Name the parasite shown.
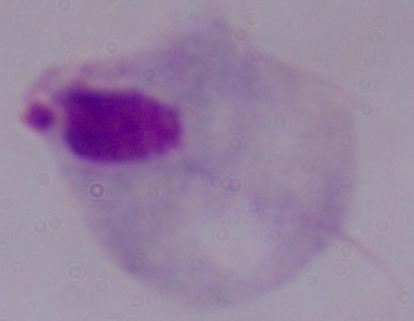

This is a trichomonad.

Summary:
  - Magnification: 1000x
  - Modality: photomicrograph